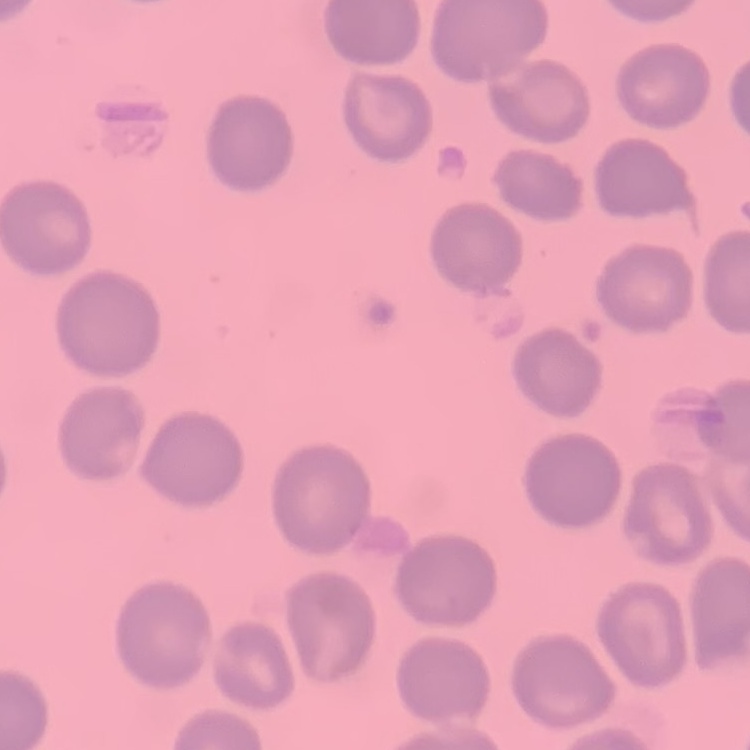
The erythrocytes exhibit no rouleaux formation. Thin blood smear. Square crop of a larger photomicrograph. Stained with either Field's or Giemsa.